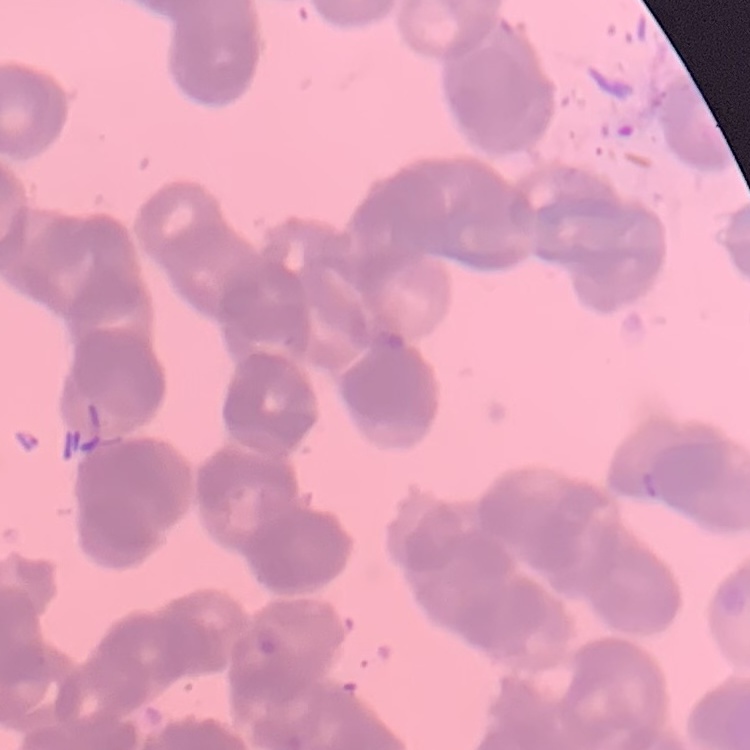

Summary:
  - Red blood cell morphology: rouleaux formation
  - Preparation: thin peripheral smear
  - Image type: one tile cut from a larger photomicrograph
  - Stain: Field's or Giemsa